Classify this cell by malaria status.
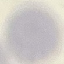

Uninfected.

Automatically extracted cell patch, resized to 64 × 64 pixels. Thin smear of blood. Photographed with a smartphone camera at the microscope eyepiece. Giemsa stain.